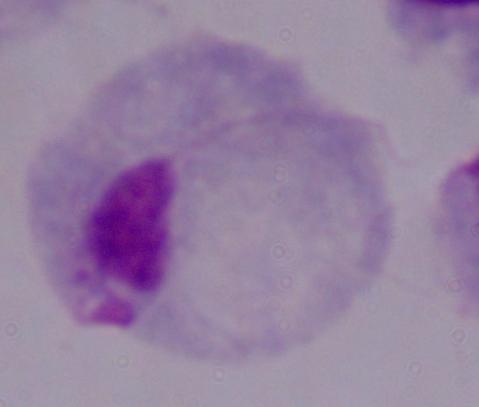

identification: trichomonad
magnification: 1000x
modality: micrograph